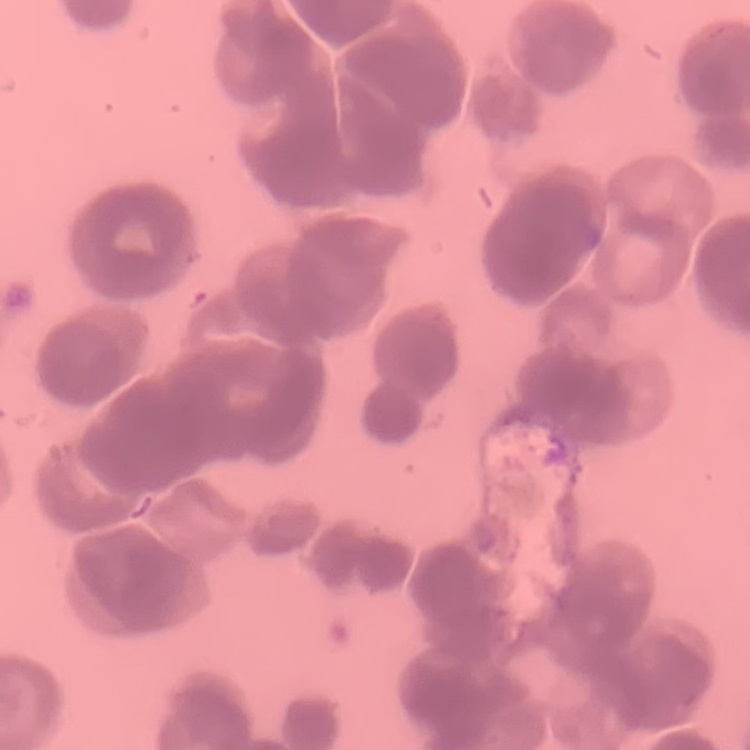
Summary:
  - Erythrocyte morphology: rouleaux formation
  - Stain: Field's or Giemsa
  - Image type: one tile cut from a larger photomicrograph
  - Preparation: thin blood film